Classify this cell by malaria status.
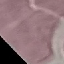
It is uninfected.

capture = smartphone through the microscope eyepiece
stain = Giemsa
preparation = thin blood film
image type = cell patch, automatically extracted from a larger field of view and resized to 64 × 64 pixels